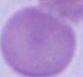
modality: photomicrograph
magnification: 1000x
identification: red blood cell